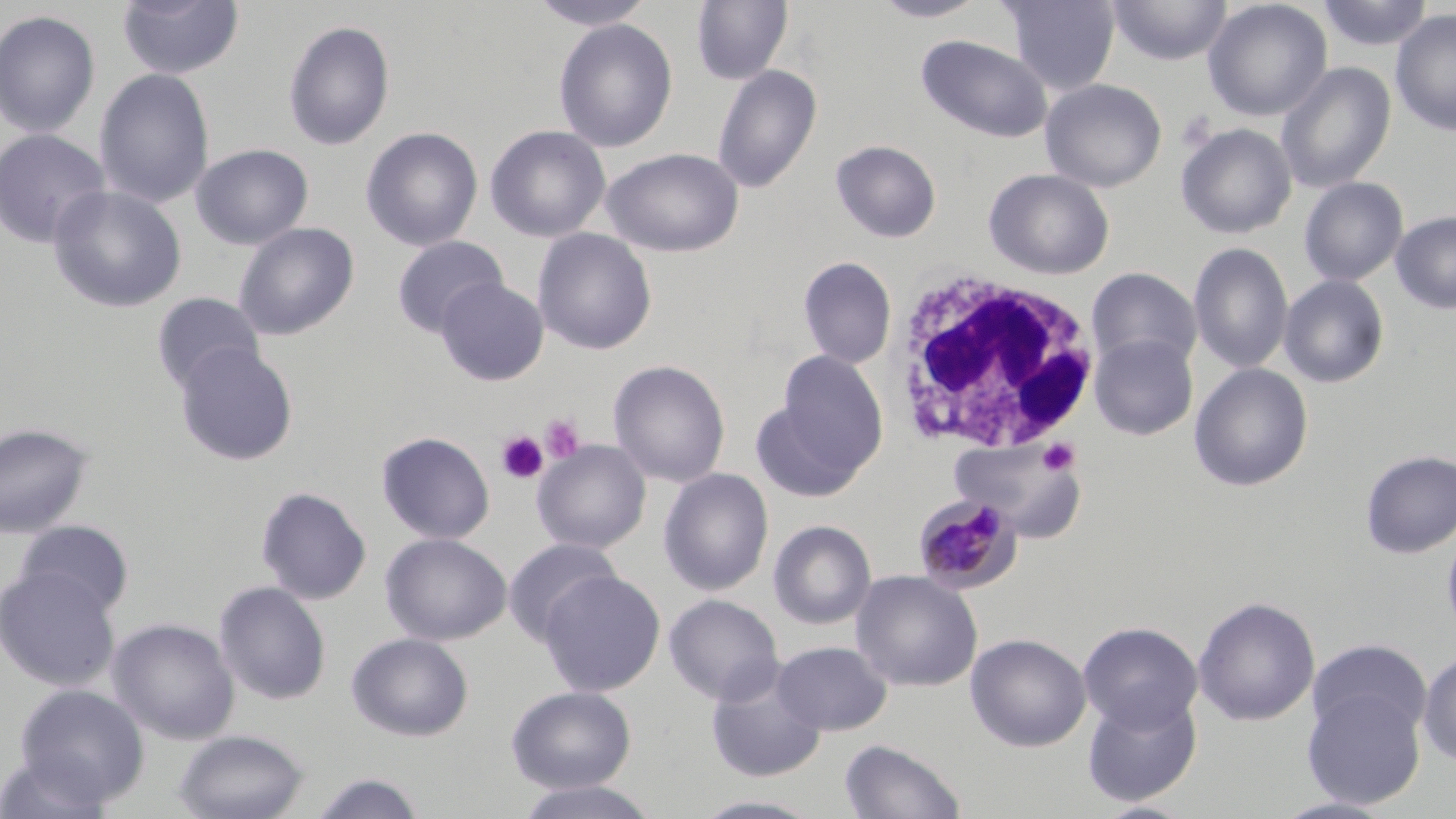

Approximate bounding boxes as [x1, y1, x2, y2] in pixels. Uninfected red blood cell locations: [117, 0, 245, 80], [530, 0, 655, 31], [691, 0, 793, 85], [868, 0, 992, 22], [1000, 0, 1120, 94], [1106, 0, 1232, 66], [1202, 0, 1333, 122], [1316, 0, 1434, 51], [1390, 8, 1456, 137], [0, 9, 101, 139], [553, 18, 678, 153], [283, 20, 395, 150], [917, 35, 1053, 143], [1276, 61, 1396, 194], [712, 64, 823, 193], [94, 68, 215, 208], [1040, 79, 1167, 193], [1175, 123, 1297, 239], [485, 124, 611, 243], [361, 127, 483, 251], [0, 129, 110, 249], [830, 139, 942, 243], [191, 143, 313, 250], [602, 148, 744, 256], [984, 168, 1115, 279], [1299, 177, 1408, 286], [48, 184, 186, 313], [1391, 211, 1456, 315], [234, 222, 359, 340], [532, 228, 657, 355], [392, 235, 507, 336], [1189, 242, 1294, 374], [797, 256, 897, 368], [1086, 268, 1202, 372], [1278, 275, 1389, 388], [436, 277, 549, 386], [152, 291, 266, 393], [1088, 333, 1198, 440], [174, 343, 299, 466], [775, 349, 889, 480], [608, 359, 730, 487], [1189, 363, 1313, 492], [749, 395, 866, 503], [0, 423, 95, 539], [376, 431, 495, 544], [949, 438, 1087, 542], [532, 440, 651, 554], [1360, 449, 1456, 559], [658, 468, 774, 596], [256, 486, 371, 604], [768, 519, 876, 630], [13, 520, 135, 618], [1442, 525, 1456, 644], [380, 532, 511, 646], [502, 538, 624, 646], [0, 566, 120, 692], [538, 569, 666, 696], [850, 570, 983, 692], [214, 580, 331, 705], [664, 594, 784, 706], [1193, 595, 1321, 727], [108, 617, 239, 745], [1078, 621, 1203, 733], [347, 632, 474, 741], [966, 633, 1091, 752], [1307, 638, 1432, 745], [772, 640, 892, 735], [1418, 650, 1456, 766], [706, 667, 827, 783], [15, 684, 149, 807], [506, 685, 637, 793], [1301, 687, 1425, 810], [1082, 692, 1202, 807], [174, 728, 310, 819], [839, 738, 967, 819], [0, 750, 115, 819], [306, 772, 428, 819], [512, 780, 661, 819], [689, 794, 827, 818], [1272, 796, 1399, 818]. Plasmodium malariae-infected red blood cell locations: [914, 494, 1020, 594]. Platelet locations: [1176, 111, 1218, 151], [540, 413, 586, 463], [497, 431, 548, 484], [1037, 437, 1080, 476]. White blood cell locations: [885, 270, 1101, 455]. Slide-level diagnosis: Plasmodium malariae. Captured at 1000x magnification. May-Grünwald-Giemsa-stained preparation. Thin blood film. Light microscopy. Image is 1456×819 pixels. One field of a larger specimen.